Name the cell type shown.
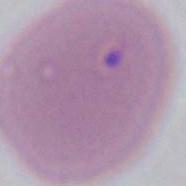
An erythrocyte.

Captured at 1000x magnification. Photomicrograph.